Classify this cell by malaria status.
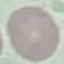
It is uninfected.

Summary:
  - Preparation: thin blood smear
  - Capture: smartphone camera at the microscope eyepiece
  - Image type: automatically extracted cell patch, resized to 64 × 64 pixels
  - Stain: Giemsa